Report the malaria status of this cell.
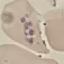

Uninfected.

image type = cell patch, automatically extracted from a larger field of view and resized to 64 × 64 pixels
preparation = thin blood film
stain = Giemsa
capture = smartphone camera at the microscope eyepiece